Describe the morphology of the erythrocytes.
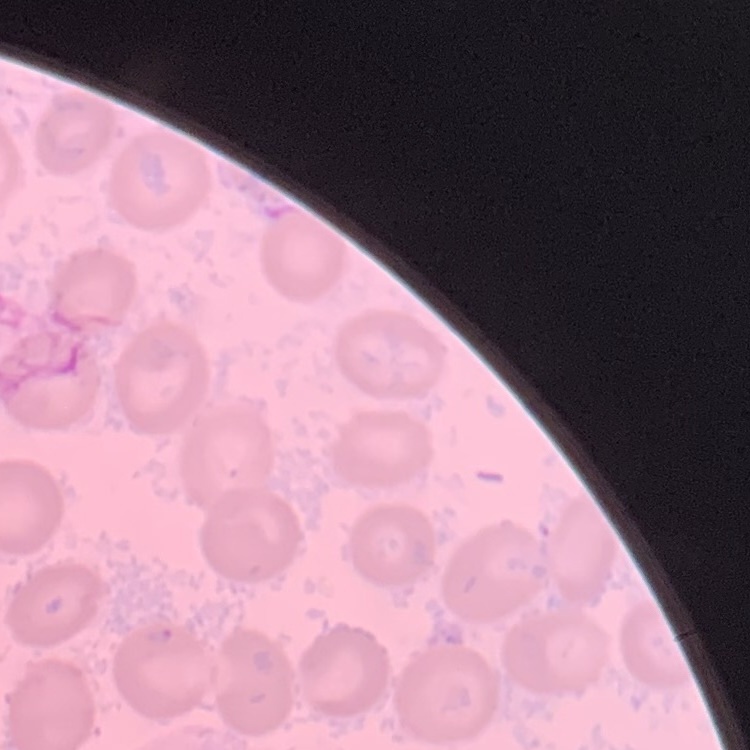

No rouleaux formation.

Summary:
  - Image type: square crop of a larger photomicrograph
  - Preparation: thin blood film
  - Stain: Field's or Giemsa